Report the malaria status of this cell.
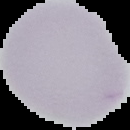

Uninfected.

{
  "image_type": "cell region segmented out of the field of view; surrounding area masked to black",
  "preparation": "thin blood film",
  "image_size": "130×130 pixels"
}